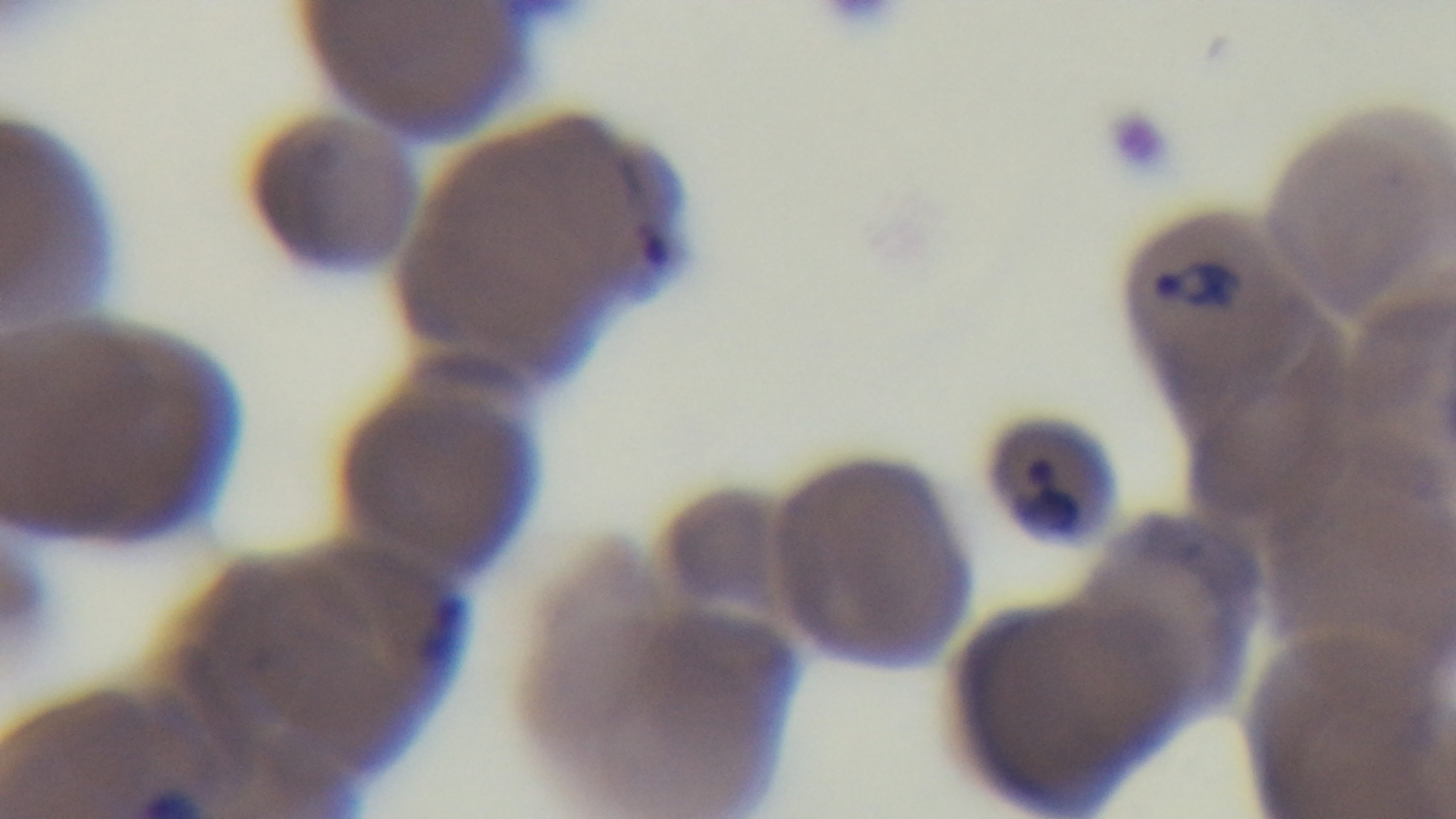
{
  "modality": "light microscopy",
  "field_of_view": "single",
  "preparation": "thin blood film",
  "capture": "mounted 4K digital camera",
  "malaria_status": "positive",
  "stain": "Giemsa",
  "objective": "100x oil immersion"
}